Report the malaria status of this cell.
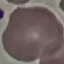

It is uninfected.

Summary:
  - Preparation: thin smear
  - Stain: Giemsa
  - Capture: smartphone through the microscope eyepiece
  - Image type: automatically extracted cell patch, resized to 64 × 64 pixels